State which parasite is depicted.
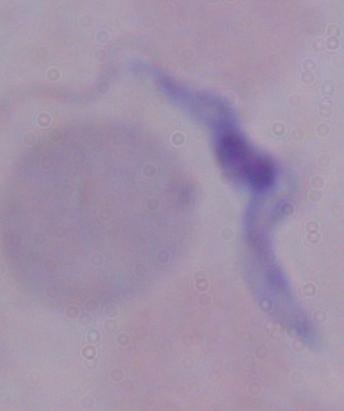
This is a trypanosome.

Photomicrograph. Captured at 1000x magnification.